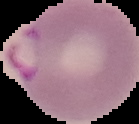

{
  "image_type": "cell region segmented out of the field of view; surrounding area masked to black",
  "malaria_status": "parasitized",
  "preparation": "thin blood smear",
  "image_size": "139×124 pixels"
}